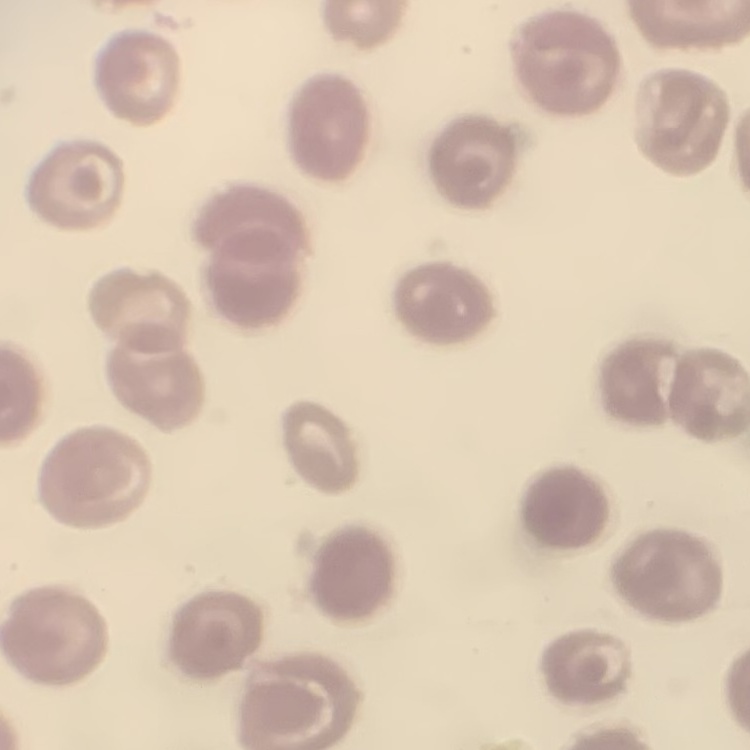 The erythrocytes show no rouleaux formation. Thin peripheral smear. One tile cut from a larger photomicrograph. Stained with either Field's or Giemsa.